Point out malaria parasites and leukocytes.
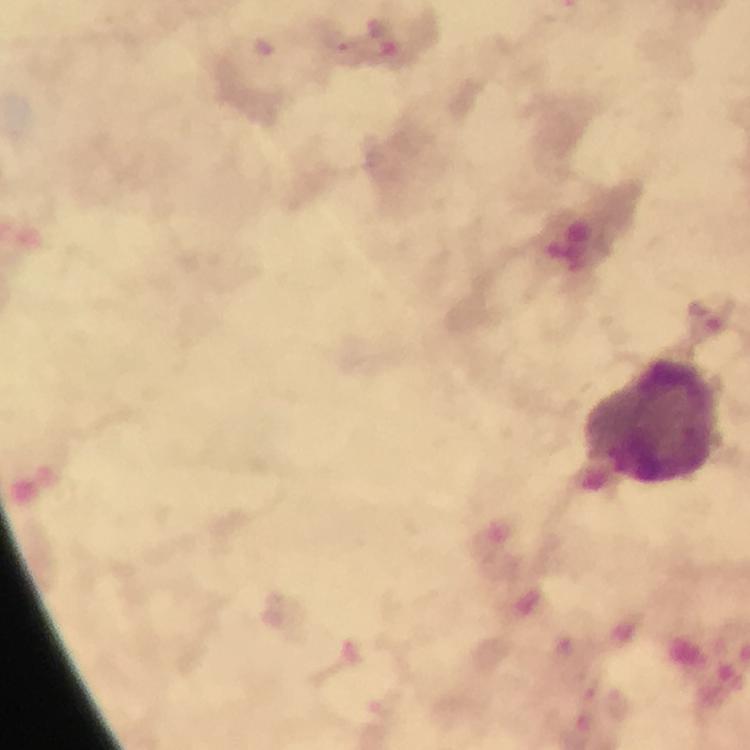
Approximate centers as [x, y] in pixels.
Malaria parasites: [337, 41].
Leukocytes: [651, 421].

Summary:
  - Preparation: thick blood smear
  - Stain: Giemsa
  - Capture: smartphone mounted on the microscope
  - Magnification: 100x
  - Immersion oil: applied
  - Cropped from: one field of view
  - Image size: 750×750 pixels
  - Context: from a malaria diagnostic workup